Give the extent of all white blood cells.
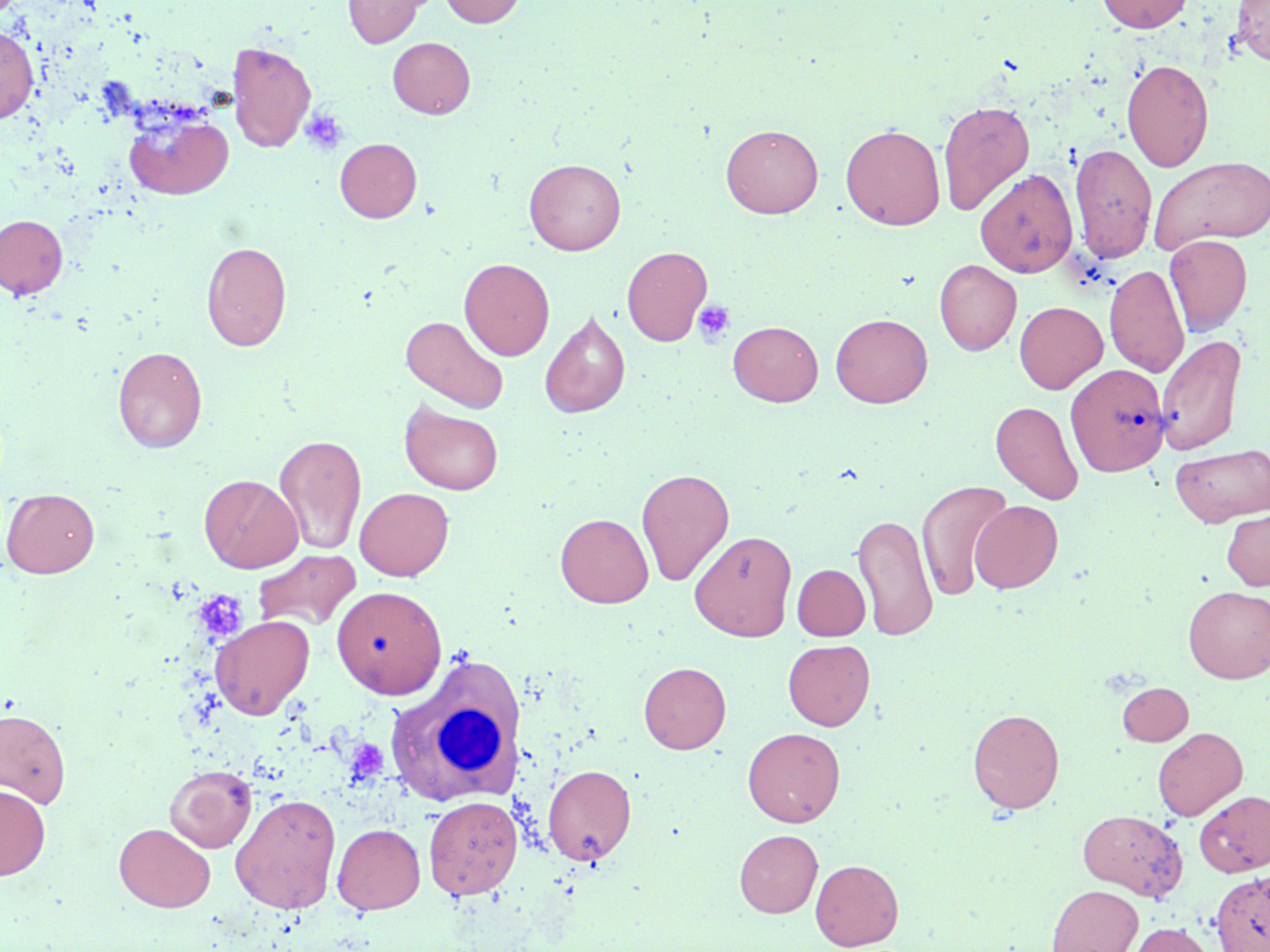
Approximate bounding boxes as named x1/y1/x2/y2 corners in pixels.
White blood cells: (x1=384, y1=657, x2=524, y2=810).

Uninfected red blood cell locations: (x1=343, y1=0, x2=426, y2=47), (x1=439, y1=0, x2=526, y2=27), (x1=1097, y1=0, x2=1193, y2=33), (x1=1232, y1=0, x2=1270, y2=66), (x1=0, y1=25, x2=38, y2=124), (x1=388, y1=37, x2=475, y2=118), (x1=227, y1=41, x2=317, y2=152), (x1=1121, y1=59, x2=1214, y2=171), (x1=937, y1=99, x2=1035, y2=216), (x1=123, y1=110, x2=233, y2=200), (x1=721, y1=124, x2=823, y2=218), (x1=841, y1=124, x2=945, y2=230), (x1=335, y1=138, x2=422, y2=222), (x1=1069, y1=143, x2=1158, y2=263), (x1=1149, y1=156, x2=1270, y2=253), (x1=524, y1=158, x2=626, y2=255), (x1=976, y1=169, x2=1078, y2=277), (x1=0, y1=214, x2=68, y2=299), (x1=1164, y1=234, x2=1252, y2=335), (x1=201, y1=241, x2=292, y2=352), (x1=622, y1=245, x2=712, y2=346), (x1=459, y1=258, x2=555, y2=360), (x1=934, y1=259, x2=1021, y2=355), (x1=1105, y1=263, x2=1189, y2=378), (x1=1014, y1=301, x2=1107, y2=393), (x1=539, y1=310, x2=631, y2=419), (x1=831, y1=314, x2=933, y2=407), (x1=400, y1=315, x2=510, y2=415), (x1=728, y1=321, x2=823, y2=406), (x1=1156, y1=334, x2=1246, y2=455), (x1=113, y1=346, x2=207, y2=453), (x1=1066, y1=363, x2=1170, y2=476), (x1=400, y1=401, x2=504, y2=495), (x1=991, y1=401, x2=1083, y2=504), (x1=273, y1=433, x2=367, y2=555), (x1=1171, y1=443, x2=1270, y2=527), (x1=636, y1=467, x2=734, y2=586), (x1=199, y1=474, x2=303, y2=573), (x1=916, y1=480, x2=1013, y2=601), (x1=355, y1=487, x2=454, y2=581), (x1=2, y1=488, x2=99, y2=578), (x1=970, y1=500, x2=1063, y2=593), (x1=1221, y1=508, x2=1270, y2=590), (x1=853, y1=512, x2=938, y2=641), (x1=555, y1=513, x2=653, y2=608), (x1=689, y1=530, x2=796, y2=641), (x1=253, y1=549, x2=362, y2=632), (x1=792, y1=564, x2=870, y2=640), (x1=331, y1=585, x2=446, y2=698), (x1=1183, y1=586, x2=1270, y2=683), (x1=210, y1=614, x2=314, y2=719), (x1=783, y1=639, x2=874, y2=730), (x1=639, y1=662, x2=731, y2=753), (x1=1118, y1=682, x2=1193, y2=745), (x1=0, y1=708, x2=71, y2=809), (x1=967, y1=708, x2=1064, y2=813), (x1=742, y1=727, x2=844, y2=826), (x1=1153, y1=727, x2=1247, y2=821), (x1=164, y1=764, x2=257, y2=852), (x1=543, y1=764, x2=637, y2=865), (x1=0, y1=784, x2=50, y2=880), (x1=1195, y1=790, x2=1270, y2=876), (x1=230, y1=793, x2=341, y2=913), (x1=423, y1=795, x2=522, y2=900), (x1=1077, y1=808, x2=1187, y2=900), (x1=114, y1=823, x2=215, y2=912), (x1=332, y1=823, x2=425, y2=914), (x1=734, y1=829, x2=823, y2=917), (x1=810, y1=859, x2=904, y2=950), (x1=1210, y1=870, x2=1270, y2=952), (x1=1046, y1=884, x2=1143, y2=952), (x1=1127, y1=922, x2=1214, y2=952). Platelet locations: (x1=300, y1=109, x2=349, y2=156), (x1=692, y1=300, x2=736, y2=346), (x1=195, y1=591, x2=247, y2=640). Slide-level diagnosis: no evidence of blood parasites. 1000x magnification. May-Grünwald-Giemsa-stained preparation. Thin blood film. Image is 1270×952 pixels. Light microscopy. Single field of view.